State which parasite is depicted.
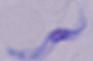

A trypanosome.

Micrograph. 1000x magnification.